Name the parasite shown.
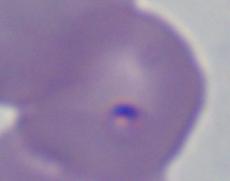
Babesia.

modality = micrograph
magnification = 1000x